State which parasite is depicted.
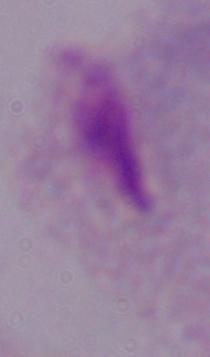

A trichomonad.

Captured at 1000x magnification. Micrograph.